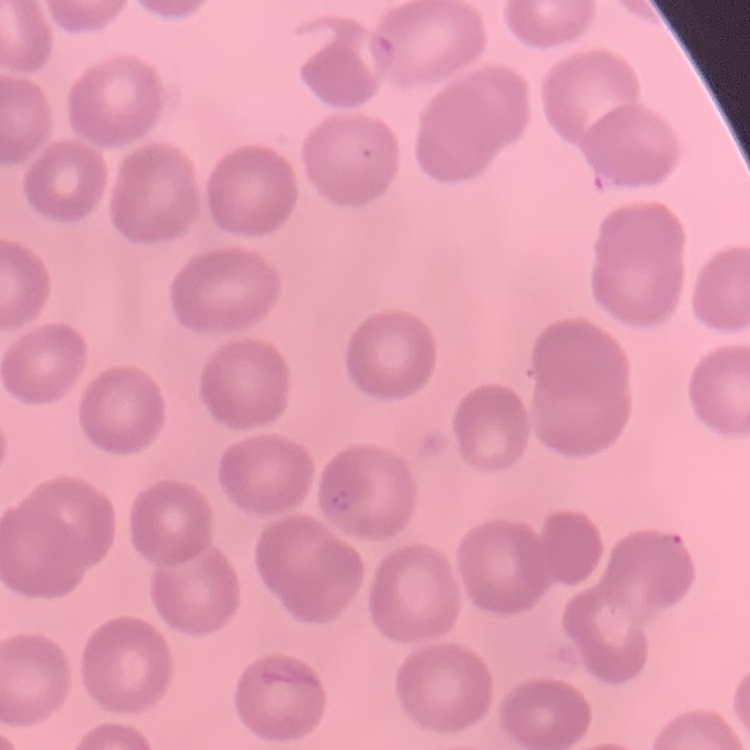

Summary:
  - Erythrocyte morphology: no rouleaux formation
  - Stain: Field's or Giemsa
  - Image type: square crop of a larger photomicrograph
  - Preparation: thin blood smear